Name the cell type shown.
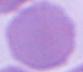

An erythrocyte.

magnification = 1000x
modality = photomicrograph